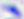

{
  "identification": "Toxoplasma gondii",
  "magnification": "400x",
  "modality": "micrograph"
}